Comment on the morphology of the red blood cells.
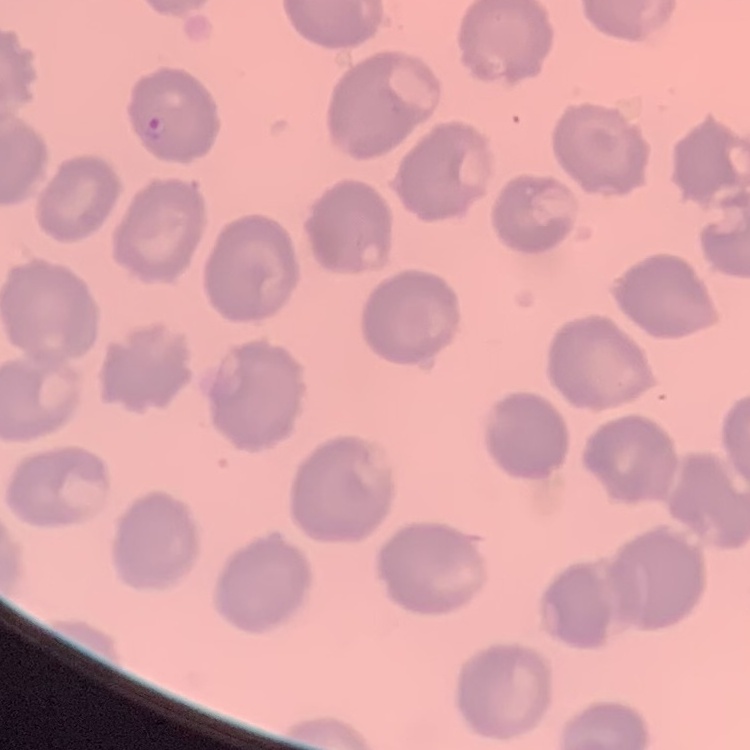

They show no rouleaux formation.

Summary:
  - Preparation: thin peripheral smear
  - Image type: square crop of a larger photomicrograph
  - Stain: Field's or Giemsa